Classify the preparation.
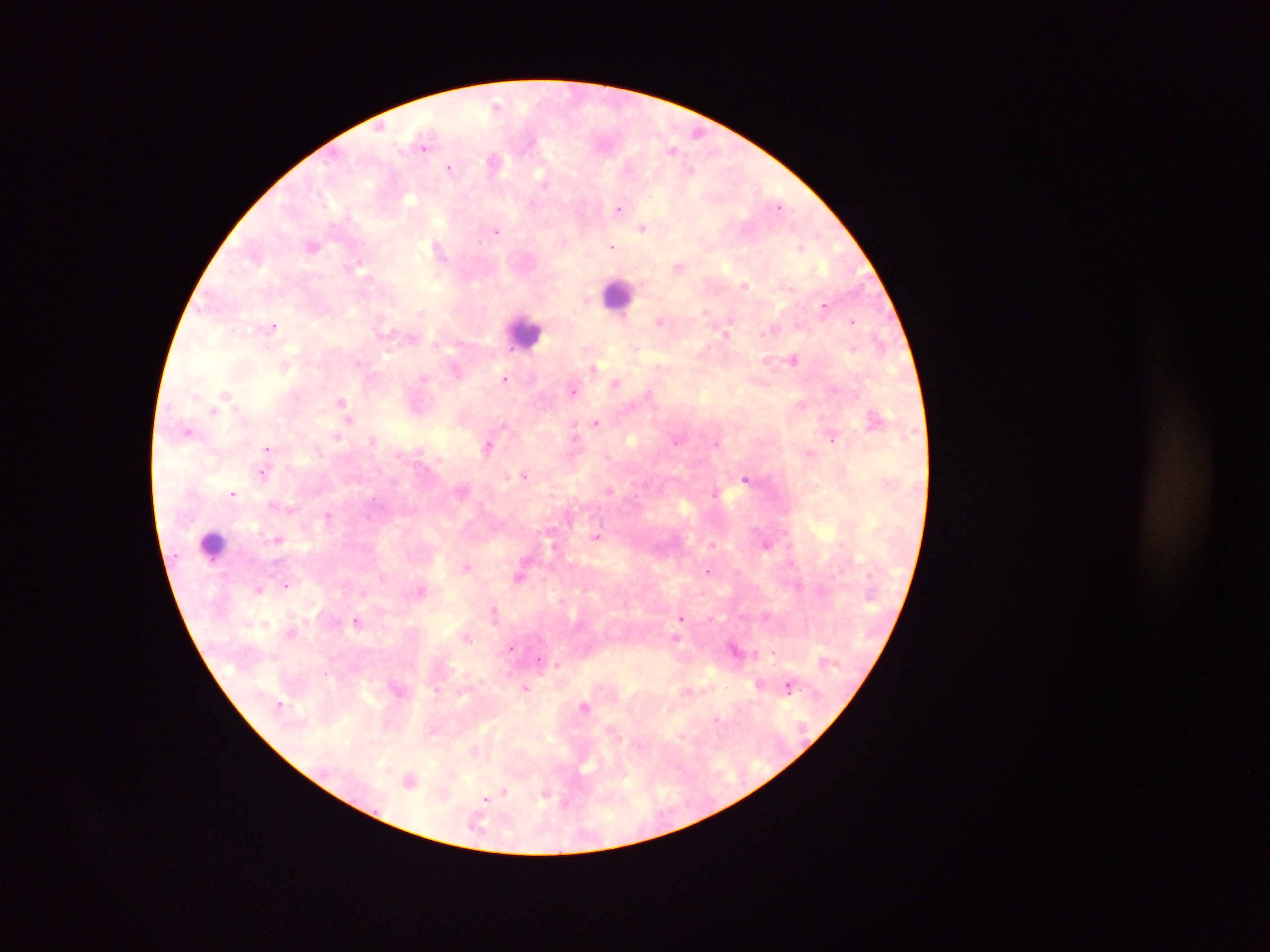
Thick blood smear.

Approximate centers as (x, y) in pixels. Plasmodium parasite locations: (497, 104), (698, 131), (424, 147), (672, 149), (494, 162), (450, 168), (690, 170), (543, 183), (779, 206), (619, 208), (643, 227), (497, 231), (312, 246), (612, 246), (438, 248), (801, 248), (359, 262), (678, 266), (745, 285), (825, 306), (704, 312), (421, 313), (659, 321), (853, 321), (273, 326), (767, 332), (725, 333), (793, 360), (658, 366), (595, 368), (506, 379), (616, 383), (572, 391), (225, 393), (649, 393), (342, 402), (801, 404), (214, 411), (349, 420), (596, 422), (504, 424), (188, 432), (573, 434), (338, 436), (833, 439), (373, 440), (676, 442), (716, 443), (488, 445), (267, 448), (809, 454), (262, 473), (524, 474), (745, 478), (610, 491), (715, 492), (233, 494), (328, 514), (596, 537), (278, 540), (713, 545), (467, 566), (708, 571), (520, 576), (285, 585), (260, 589), (420, 591), (494, 610), (680, 618), (357, 621), (676, 638), (467, 639), (511, 648), (538, 660), (557, 664), (759, 684), (788, 687), (526, 688), (280, 704), (585, 706), (717, 718), (410, 781), (504, 792), (496, 794), (544, 795), (486, 798). Leukocyte locations: (619, 294), (525, 332), (213, 546). Image is 1270×952 pixels. Photographed through a microscope with a mobile-phone camera. Sample from Ghana. Single field of view.